Assess this cell for malaria.
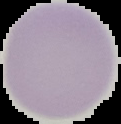
It is uninfected.

preparation = thin blood film
image size = 121×124 pixels
image type = segmented cell region on a black background